Report the malaria status of this cell.
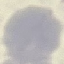

It is uninfected.

image type = cell patch, automatically extracted from a larger field of view and resized to 64 × 64 pixels
preparation = thin blood smear
capture = smartphone through the microscope eyepiece
stain = Giemsa